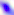
magnification = 400x
modality = photomicrograph
identification = Toxoplasma gondii